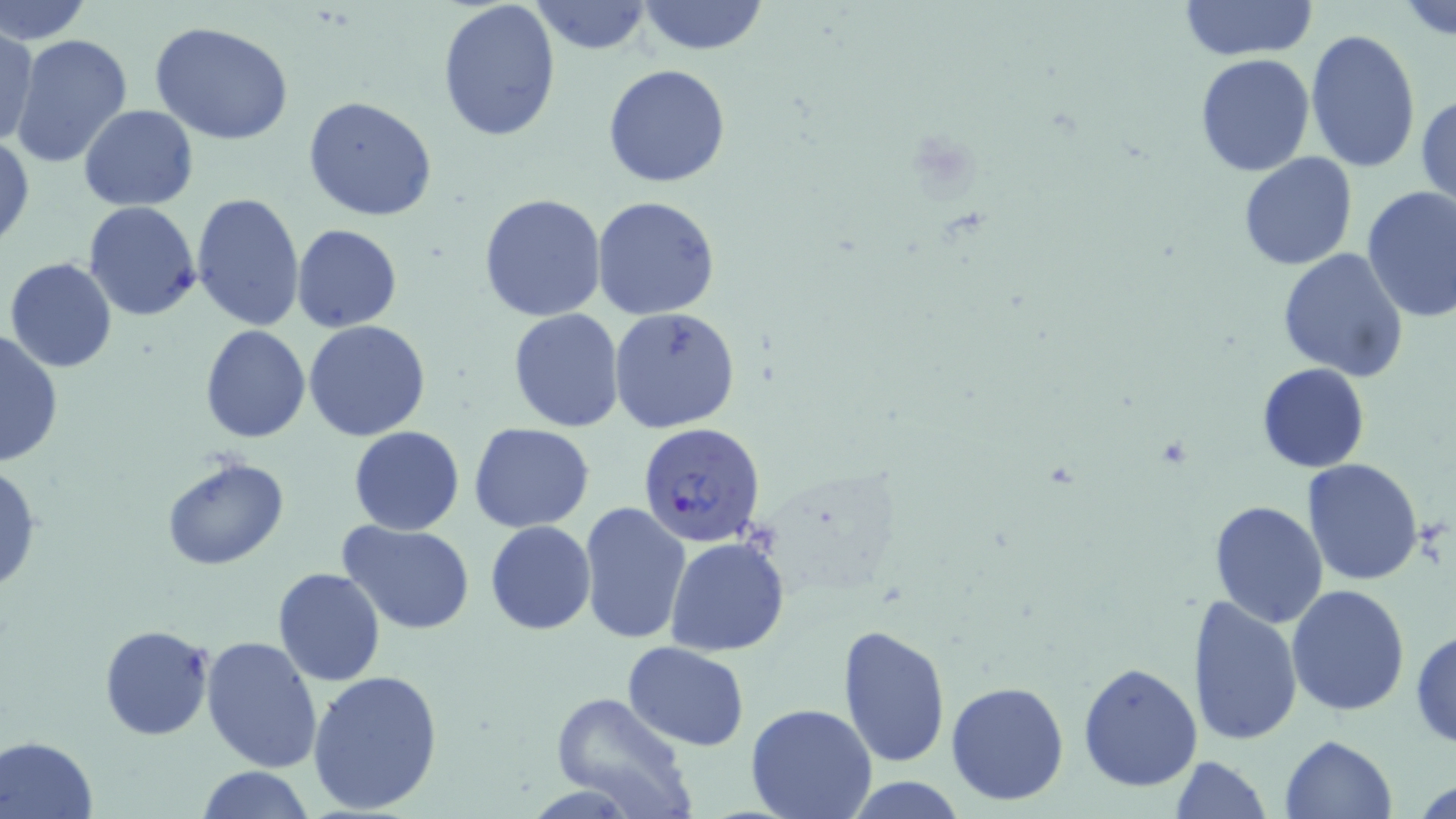

Summary:
  - Coordinate format: approximate bounding boxes as (x1, y1, x2, y2) in pixels
  - Uninfected red blood cell locations (subset): (0, 0, 90, 48), (531, 0, 652, 56), (637, 0, 769, 56), (1178, 0, 1316, 61), (436, 1, 561, 141), (1398, 1, 1456, 39), (149, 21, 296, 146), (1, 27, 40, 148), (1304, 28, 1422, 173), (8, 33, 134, 170), (1194, 56, 1315, 176), (603, 63, 731, 187), (1416, 91, 1456, 210), (304, 97, 438, 223), (80, 105, 198, 212), (0, 131, 34, 255), (1238, 152, 1358, 272), (1360, 185, 1456, 323), (191, 191, 304, 329), (478, 193, 607, 323), (591, 195, 722, 321), (83, 200, 201, 321), (291, 224, 403, 332), (1276, 249, 1409, 381), (4, 257, 119, 372), (608, 308, 741, 433), (506, 310, 625, 432), (304, 320, 432, 441), (201, 325, 310, 443), (0, 329, 62, 469), (1258, 364, 1369, 473), (469, 421, 596, 532), (349, 425, 464, 534), (160, 454, 290, 571), (1301, 457, 1425, 585), (0, 465, 43, 595), (1207, 500, 1328, 629), (578, 501, 693, 645), (337, 521, 478, 637), (485, 521, 597, 635), (665, 535, 791, 657), (272, 567, 386, 688), (1286, 585, 1411, 717), (1188, 594, 1303, 746), (99, 625, 215, 740), (839, 625, 952, 769), (1410, 628, 1456, 746), (202, 636, 324, 775), (623, 642, 749, 749), (1078, 660, 1202, 792), (308, 671, 445, 815), (946, 681, 1069, 805), (547, 690, 697, 819), (745, 702, 877, 819), (1, 735, 99, 818), (1280, 735, 1398, 819), (1169, 755, 1272, 819), (195, 766, 317, 819), (841, 774, 969, 817)
  - Slide-level diagnosis: Plasmodium falciparum
  - Field of view: single
  - Image size: 1456×819 pixels
  - Magnification: 1000x
  - Modality: light microscopy
  - Preparation: thin blood smear
  - Stain: May-Grünwald-Giemsa